Comment on the morphology of the red blood cells.
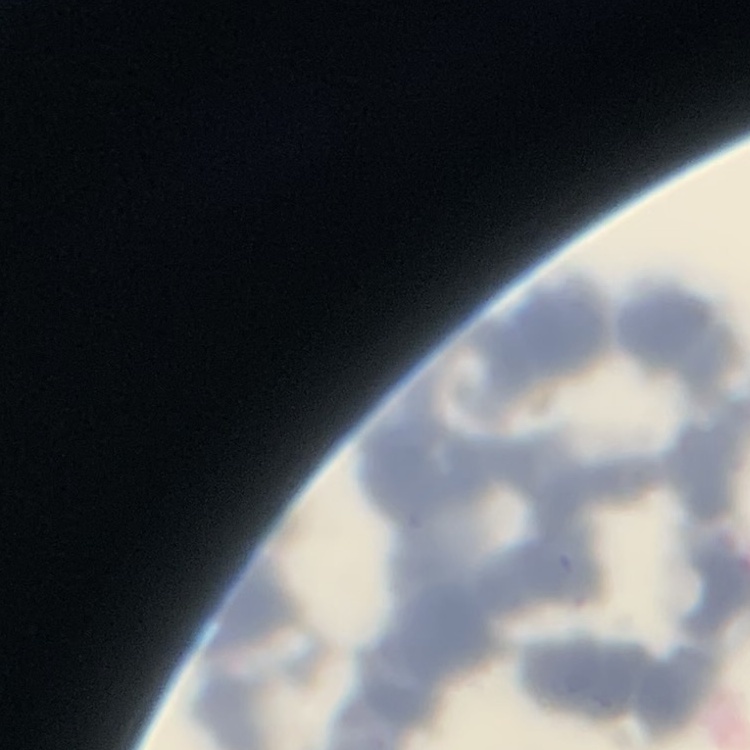
Rouleaux formation.

Stained with either Field's or Giemsa. Square crop of a larger photomicrograph. Thin peripheral smear.